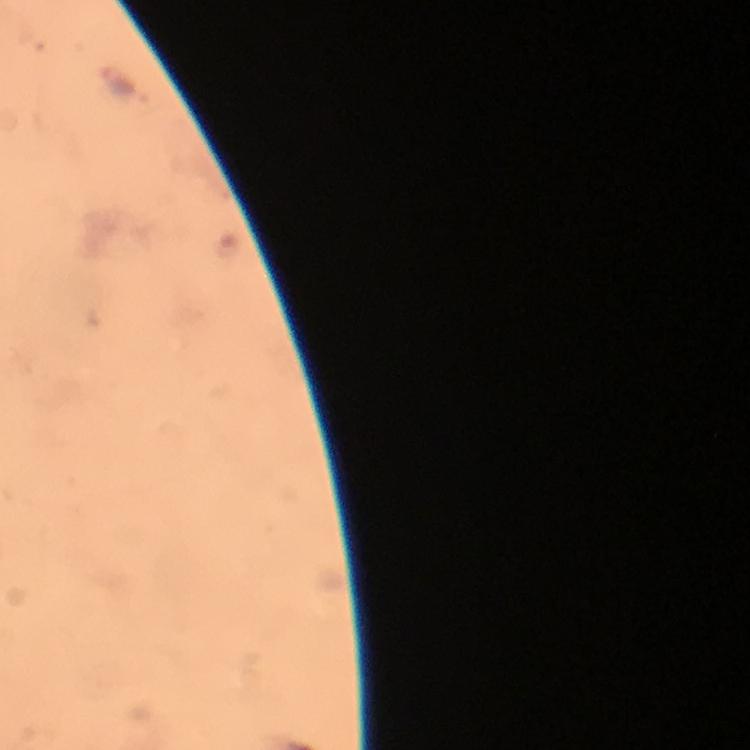
Approximate object centers, in pixels from the top-left corner.
Summary:
  - Malaria parasite locations: (x=118, y=82)
  - Immersion oil: used
  - Magnification: 100x
  - Context: from a diagnostic examination for malaria
  - Cropped from: a single field of view
  - Stain: Giemsa
  - Preparation: thick blood smear
  - Image size: 750×750 pixels
  - Capture: smartphone photograph through a microscope